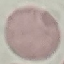

Malaria status: uninfected. Cell patch, automatically extracted from a larger field of view and resized to 64 × 64 pixels. Photographed with a smartphone camera at the microscope eyepiece. Thin smear of blood. Giemsa-stained preparation.